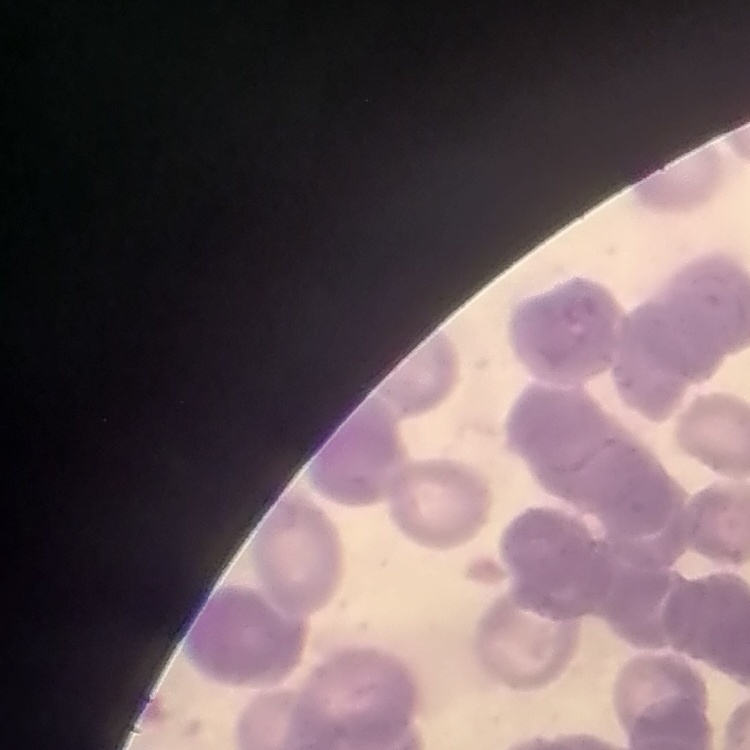

erythrocyte morphology = rouleaux formation
preparation = thin peripheral smear
stain = Field's or Giemsa
image type = one tile cut from a larger photomicrograph